Outline each blood parasite and name the species.
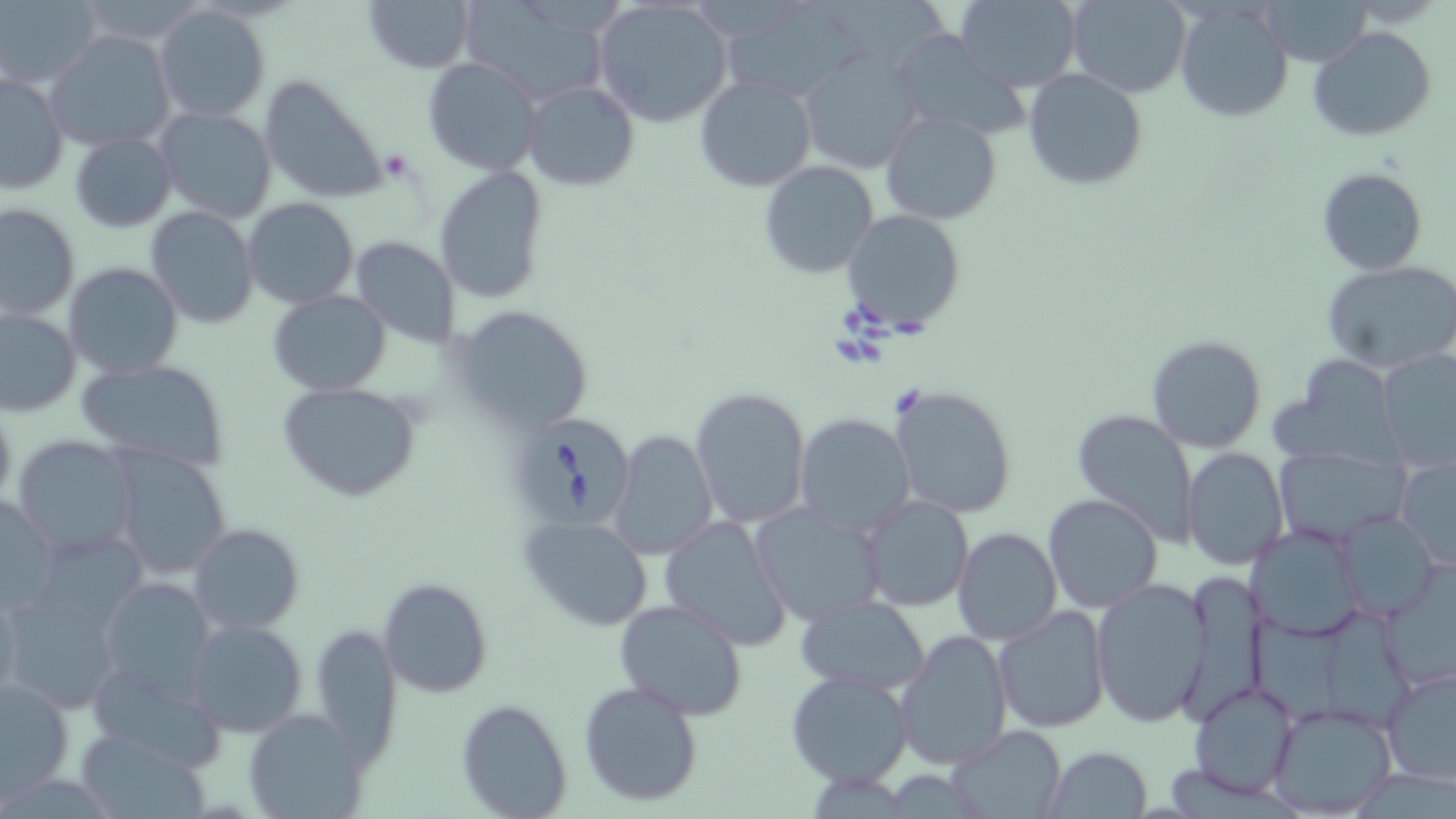
Approximate bounding boxes as (x1,y1)-(x2,y2) corner pairs in pixels.
Babesia divergens-infected red blood cells: (514,418)-(632,528).
No Plasmodium falciparum, Plasmodium ovale, Plasmodium malariae, Plasmodium vivax, or Trypanosoma brucei observed.

{
  "slide_level_diagnosis": "Babesia divergens",
  "magnification": "1000x",
  "modality": "light microscopy",
  "preparation": "thin blood smear",
  "stain": "May-Grünwald-Giemsa",
  "image_size": "1456×819 pixels",
  "field_of_view": "one of a larger specimen",
  "uninfected_red_blood_cell_locations": "approximate bounding boxes as (x1,y1)-(x2,y2) corner pairs in pixels: (362,0)-(476,73), (716,0)-(871,105), (813,0)-(944,64), (954,0)-(1082,91), (1066,0)-(1192,99), (1174,0)-(1294,122), (1262,0)-(1372,67), (1,1)-(100,88), (461,1)-(606,104), (591,1)-(737,131), (153,6)-(271,125), (1308,26)-(1438,143), (44,31)-(176,152), (891,32)-(1029,140), (796,48)-(924,174), (422,56)-(543,175), (1023,68)-(1147,190), (0,72)-(70,195), (257,73)-(388,206), (694,75)-(817,191), (521,81)-(638,192), (152,108)-(277,225), (879,109)-(1002,225), (69,131)-(176,233), (759,161)-(880,280), (433,166)-(549,304), (1316,166)-(1428,276), (243,197)-(357,308), (0,203)-(80,321), (145,206)-(259,328), (841,209)-(965,332), (351,235)-(459,343), (1323,259)-(1456,372), (62,262)-(183,381), (268,291)-(391,396), (453,306)-(594,433), (1,307)-(80,416), (1145,335)-(1267,453), (1378,350)-(1456,473), (1275,357)-(1409,467), (74,358)-(232,473), (278,381)-(423,502), (889,385)-(1018,519), (691,387)-(812,529), (1071,409)-(1201,547), (795,414)-(916,536), (609,429)-(717,559), (11,435)-(138,559), (1180,446)-(1288,570), (1270,446)-(1409,544), (110,447)-(233,582), (1395,455)-(1456,573), (0,492)-(59,611), (1043,492)-(1163,611), (860,495)-(974,611), (749,503)-(885,627), (1338,512)-(1439,623), (659,514)-(793,652), (521,516)-(653,632), (188,522)-(304,636), (1249,524)-(1366,639), (952,526)-(1062,645), (30,530)-(150,635), (1381,560)-(1456,691), (1178,574)-(1263,721), (98,577)-(216,701), (378,577)-(490,698), (1091,580)-(1213,729), (0,590)-(123,712), (796,595)-(930,692), (613,599)-(748,720), (991,605)-(1110,734), (1308,607)-(1416,732), (1246,613)-(1341,724), (184,618)-(309,739), (307,624)-(402,760), (896,629)-(1013,769), (85,658)-(228,772), (1379,666)-(1455,786), (786,669)-(913,788), (0,677)-(75,799), (578,679)-(704,805), (1189,682)-(1301,799), (457,698)-(571,818), (1266,701)-(1398,818), (245,710)-(367,818), (950,726)-(1063,816), (72,727)-(211,817), (1043,745)-(1153,817)"
}